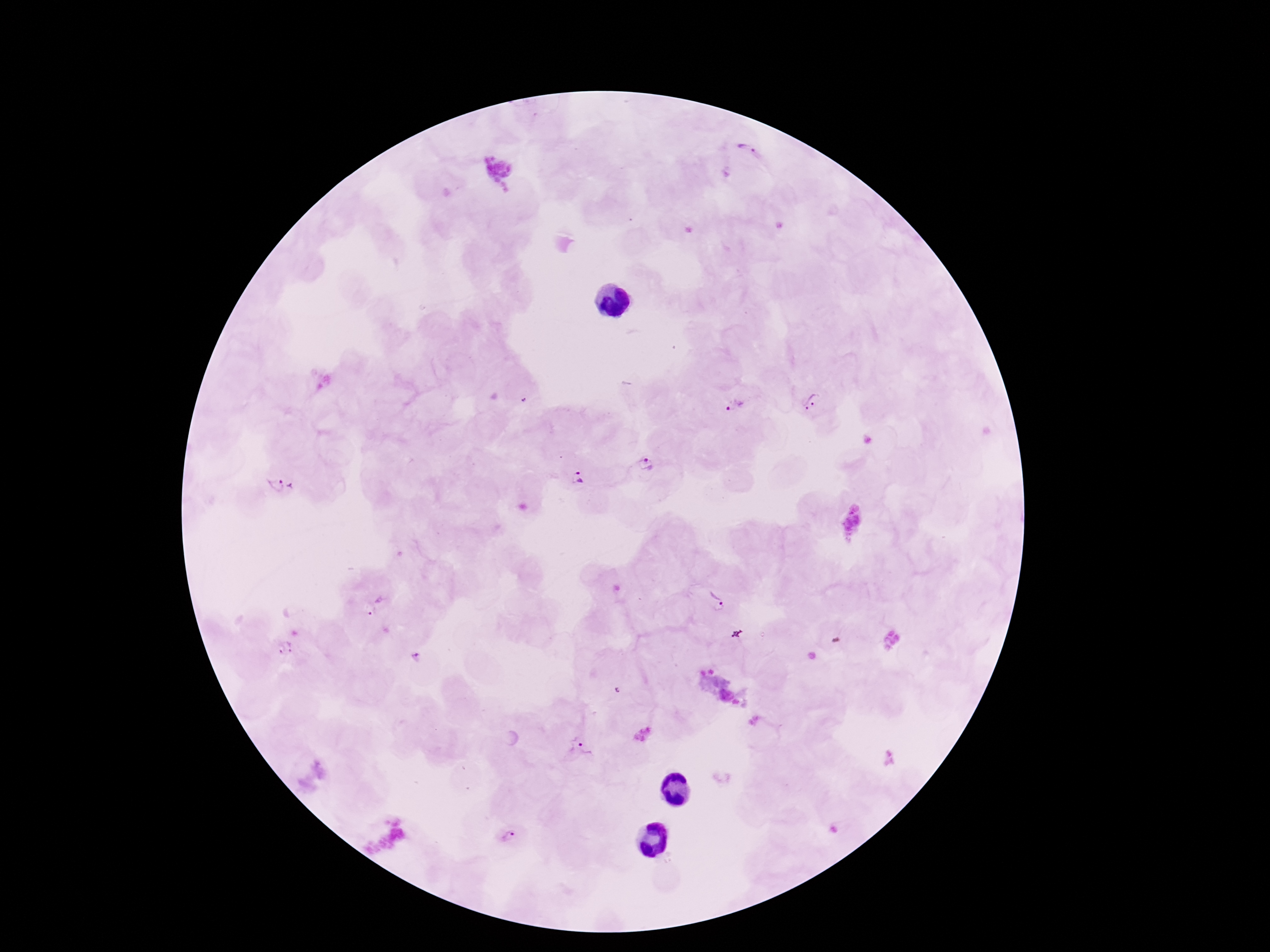

Approximate object centers, in pixels from the top-left corner. Plasmodium parasite locations: (x=748, y=149), (x=813, y=403), (x=736, y=406), (x=647, y=463), (x=577, y=477), (x=283, y=486), (x=716, y=598), (x=382, y=599), (x=369, y=609), (x=286, y=649), (x=414, y=655), (x=581, y=745), (x=506, y=838). Single field of view. Patient malaria status: positive. Thick peripheral-blood smear. Giemsa stain. Photographed through the microscope eyepiece with a smartphone camera. 100x magnification. Image is 1270×952 pixels.